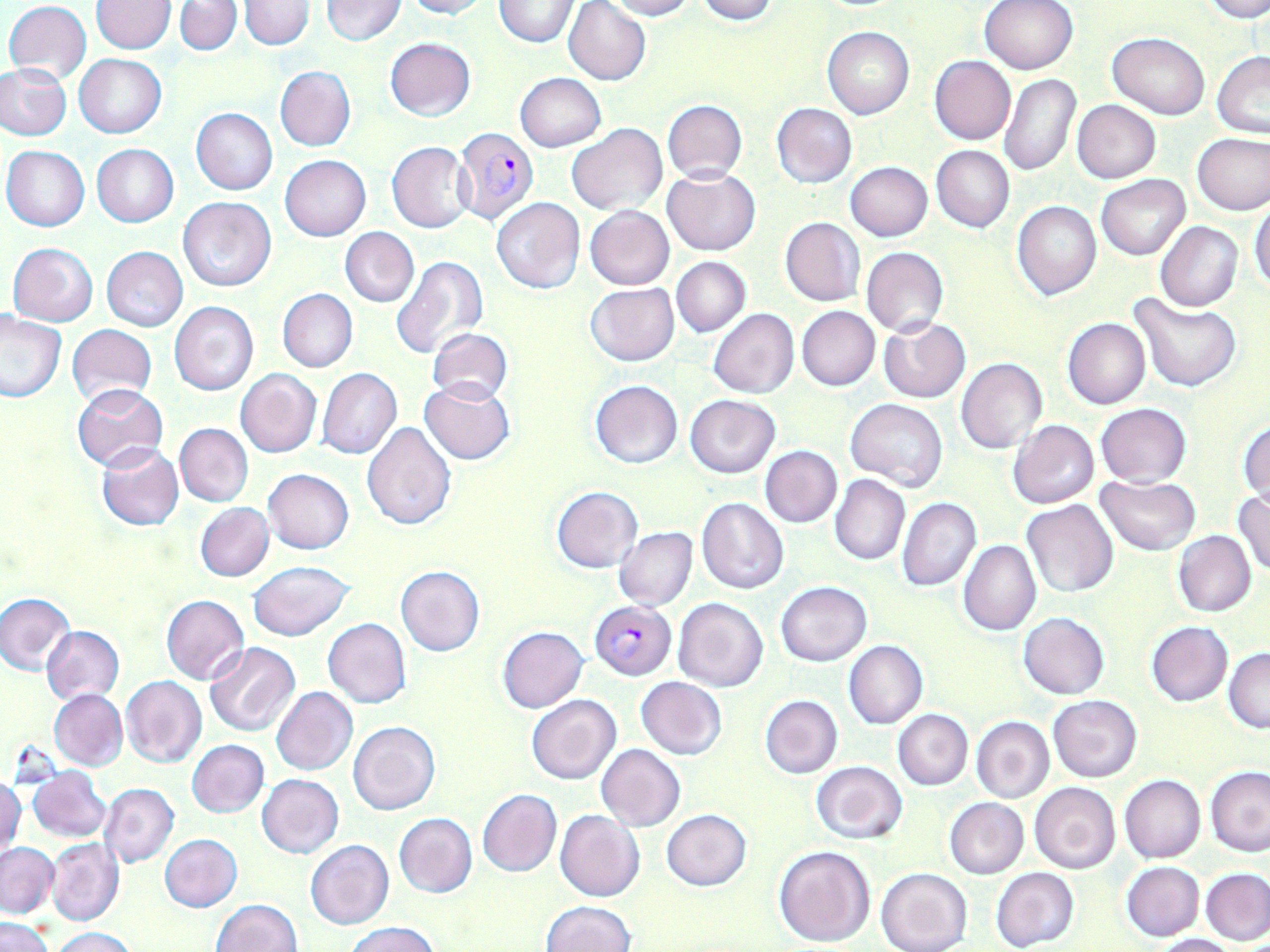

Summary:
  - Coordinate format: approximate bounding boxes as (x1,y1)-(x2,y2) corner pairs in pixels
  - Plasmodium falciparum-infected red blood cell locations: (454,127)-(539,227), (591,601)-(676,679)
  - Uninfected red blood cell locations: (321,0)-(407,45), (403,0)-(488,19), (494,0)-(577,47), (695,0)-(776,24), (979,0)-(1079,75), (1203,0)-(1270,23), (93,1)-(175,53), (176,1)-(242,54), (240,1)-(313,50), (563,1)-(651,85), (601,1)-(696,20), (4,2)-(92,83), (823,27)-(914,119), (1107,32)-(1209,119), (385,37)-(476,121), (1212,53)-(1270,137), (73,54)-(167,137), (930,55)-(1016,144), (0,63)-(73,140), (275,66)-(355,151), (515,72)-(605,152), (999,72)-(1079,176), (662,100)-(747,183), (1072,100)-(1160,183), (771,103)-(857,188), (191,109)-(277,195), (567,122)-(666,216), (1192,132)-(1270,215), (387,142)-(473,233), (91,144)-(178,227), (931,145)-(1013,232), (2,146)-(90,231), (279,155)-(370,240), (846,162)-(932,241), (662,167)-(760,257), (1097,175)-(1189,260), (179,197)-(276,291), (491,198)-(584,294), (1250,199)-(1270,292), (1013,201)-(1101,300), (584,206)-(674,290), (781,217)-(865,306), (1155,221)-(1243,312), (340,227)-(418,306), (7,242)-(97,326), (102,246)-(188,331), (861,247)-(950,337), (391,256)-(488,362), (671,257)-(750,336), (584,283)-(679,367), (277,289)-(358,373), (1130,295)-(1240,392), (169,301)-(259,397), (797,306)-(879,390), (709,309)-(799,398), (0,311)-(66,402), (1063,317)-(1150,409), (879,318)-(970,404), (67,324)-(156,405), (427,328)-(514,405), (957,359)-(1048,454), (318,368)-(401,459), (235,369)-(322,457), (419,379)-(515,465), (590,380)-(683,469), (72,382)-(169,471), (686,394)-(781,479), (846,399)-(947,491), (1096,403)-(1191,487), (1238,418)-(1269,506), (1008,421)-(1099,509), (361,422)-(456,530), (175,423)-(253,507), (96,443)-(183,531), (760,445)-(842,527), (264,469)-(354,553), (830,475)-(909,566), (1095,475)-(1202,555), (551,486)-(641,573), (1233,489)-(1270,576), (897,497)-(980,591), (696,498)-(788,594), (1022,500)-(1118,598), (194,503)-(273,581), (614,527)-(698,610), (1173,532)-(1256,617), (958,540)-(1041,636), (247,561)-(355,641), (395,566)-(485,656), (775,582)-(872,666), (0,592)-(75,675), (160,594)-(250,684), (674,598)-(768,691), (1019,613)-(1109,699), (323,618)-(412,708), (1146,621)-(1233,707), (42,625)-(124,704), (498,626)-(587,713), (844,641)-(927,729), (203,642)-(299,736), (1224,648)-(1270,733), (121,676)-(206,767), (635,677)-(728,759), (272,687)-(357,775), (49,689)-(128,770), (527,694)-(621,785), (760,694)-(843,778), (1048,695)-(1142,782), (893,709)-(972,790), (971,716)-(1054,803), (348,721)-(440,815), (187,739)-(269,817), (596,744)-(685,831), (811,760)-(909,844), (28,767)-(112,842), (1206,767)-(1270,857), (256,774)-(344,858), (1120,775)-(1206,863), (1,777)-(24,860), (1030,782)-(1121,875), (100,783)-(178,867), (478,789)-(560,876), (944,798)-(1028,879), (555,809)-(644,901), (661,809)-(751,891), (393,813)-(477,897), (159,833)-(242,912), (45,837)-(124,926), (306,839)-(394,930), (1,842)-(59,917), (773,845)-(875,948), (1121,862)-(1204,940), (991,866)-(1080,952), (877,867)-(971,952), (1201,870)-(1270,946), (211,899)-(302,952), (540,901)-(635,952), (1,917)-(53,952), (346,923)-(440,952), (54,927)-(135,952), (1152,934)-(1240,952)
  - Slide-level diagnosis: Plasmodium falciparum
  - Modality: optical microscopy
  - Preparation: thin blood film
  - Field of view: single
  - Magnification: 1000x
  - Image size: 1270×952 pixels
  - Stain: May-Grünwald-Giemsa